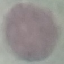
Result: negative for malaria parasites. Thin smear of blood. Automatically extracted cell patch, resized to 64 × 64 pixels. Giemsa stain. Acquired by smartphone through the microscope eyepiece.